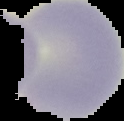
Image is 124×121 pixels. Malaria status: uninfected. From a thin blood film. Cell region segmented out of the field of view; the surrounding area is masked to black.